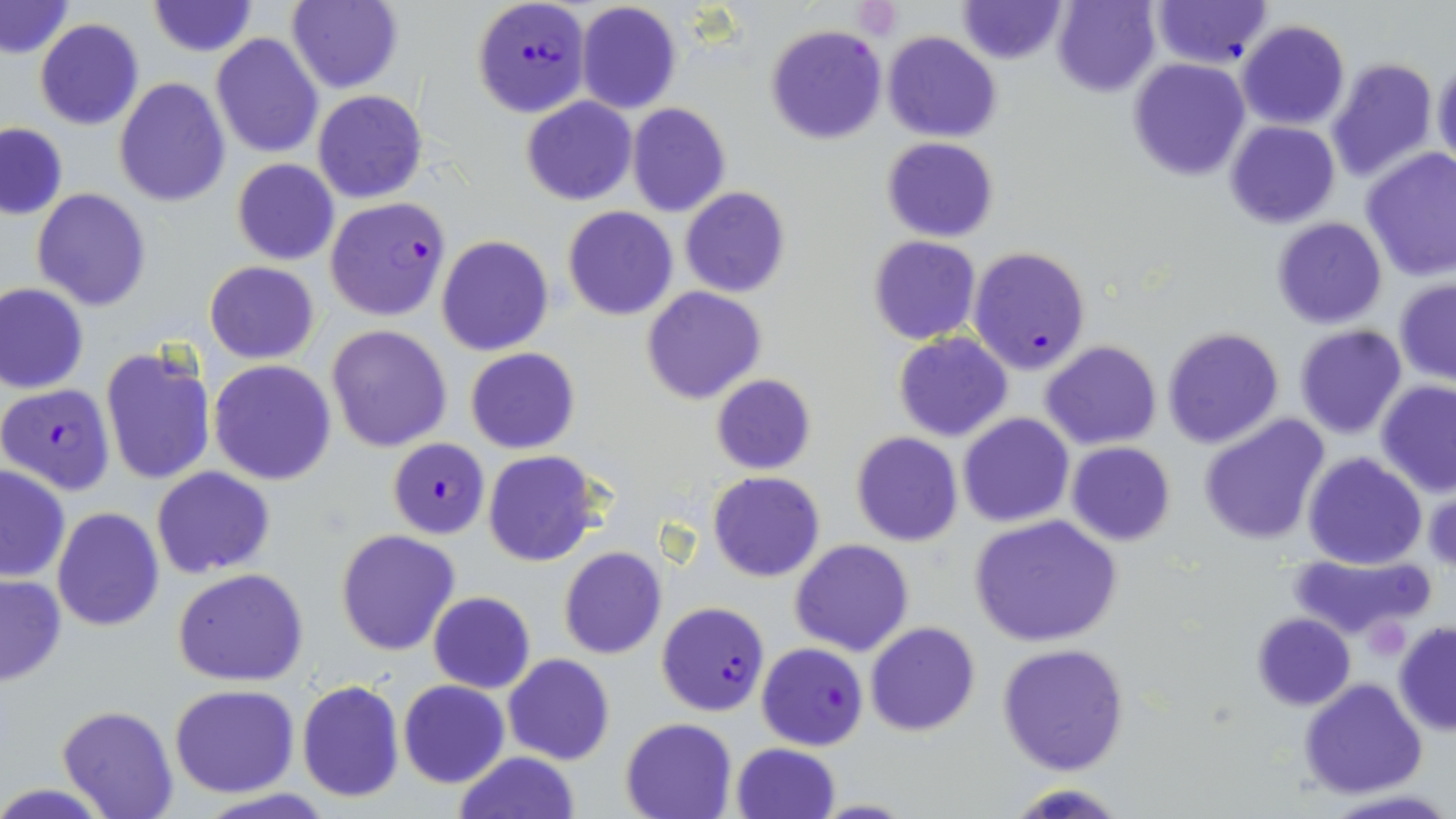 Approximate bounding boxes as (x1, y1, x2, y2) in pixels. Platelet locations: (851, 0, 901, 37). Plasmodium falciparum-infected red blood cell locations: (472, 0, 589, 117), (324, 197, 450, 321), (968, 245, 1091, 374), (0, 383, 115, 495), (386, 438, 493, 538), (657, 601, 770, 717), (757, 642, 867, 750). Uninfected red blood cell locations: (1053, 0, 1160, 96), (1151, 0, 1273, 68), (145, 1, 258, 56), (285, 1, 403, 92), (1, 2, 74, 59), (576, 2, 681, 115), (958, 2, 1067, 63), (34, 19, 145, 130), (1237, 20, 1350, 130), (765, 24, 886, 145), (881, 32, 1002, 142), (210, 35, 323, 157), (1435, 55, 1456, 170), (1127, 57, 1251, 182), (1325, 57, 1439, 184), (115, 78, 229, 206), (314, 89, 428, 203), (521, 96, 636, 205), (626, 103, 730, 217), (1225, 121, 1340, 229), (0, 123, 68, 220), (881, 137, 998, 241), (1360, 147, 1456, 281), (232, 159, 339, 266), (679, 187, 791, 298), (32, 188, 150, 311), (562, 206, 679, 320), (1270, 217, 1388, 330), (436, 235, 555, 356), (868, 235, 981, 344), (205, 261, 319, 363), (1394, 279, 1455, 384), (0, 284, 89, 395), (641, 286, 766, 404), (327, 325, 453, 451), (1294, 325, 1407, 440), (1162, 326, 1285, 449), (892, 333, 1013, 441), (1041, 341, 1162, 450), (99, 346, 216, 485), (465, 347, 579, 453), (209, 359, 337, 485), (710, 373, 816, 474), (1376, 380, 1456, 496), (958, 412, 1073, 527), (1198, 414, 1330, 545), (851, 433, 962, 546), (1066, 441, 1176, 546), (485, 452, 600, 567), (1302, 452, 1428, 570), (0, 463, 70, 584), (152, 467, 276, 578), (708, 471, 823, 582), (51, 507, 165, 631), (969, 515, 1123, 649), (335, 529, 461, 656), (789, 539, 913, 656), (559, 546, 667, 659), (1286, 552, 1435, 643), (172, 568, 309, 686), (0, 575, 67, 686), (427, 592, 536, 693), (1251, 612, 1356, 711), (1393, 621, 1456, 735), (865, 622, 980, 736), (996, 642, 1132, 776), (502, 653, 615, 765), (1299, 678, 1428, 799), (296, 679, 405, 804), (397, 680, 509, 787), (170, 684, 300, 798), (57, 703, 179, 818), (619, 717, 739, 819), (731, 742, 840, 819), (451, 751, 582, 819), (1009, 782, 1125, 818), (1324, 790, 1454, 819). Slide-level diagnosis: Plasmodium falciparum. 1000x magnification. One field of a larger specimen. Image is 1456×819 pixels. Light microscopy. Thin blood film. May-Grünwald-Giemsa stain.